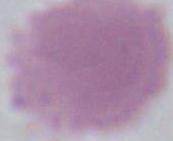 An erythrocyte is shown. 1000x magnification. Photomicrograph.